Describe the morphology of the red blood cells.
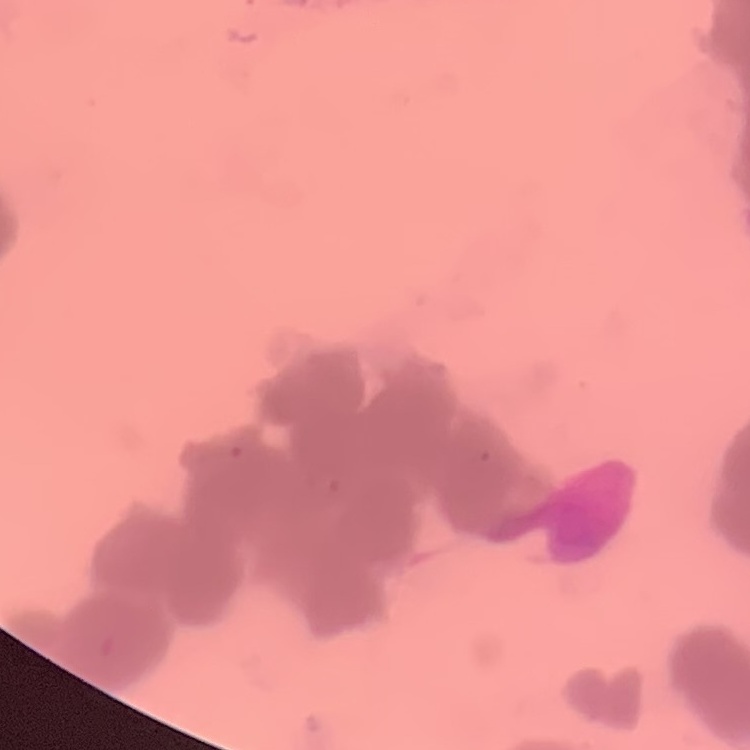
They show rouleaux formation.

preparation = thin blood smear
image type = one tile cut from a larger photomicrograph
stain = Field's or Giemsa